Locate leukocytes (white blood cells).
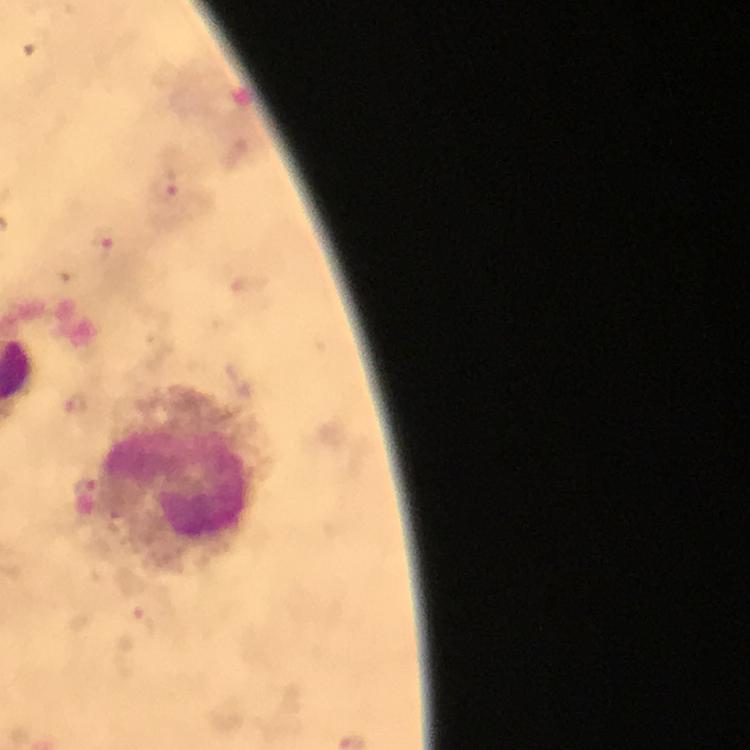

Approximate centers as {x, y} in pixels.
Leukocytes: {178, 481}.

Summary:
  - Malaria parasite locations: {164, 187}, {102, 245}, {84, 488}
  - Immersion oil: used
  - Stain: Giemsa
  - Cropped from: one field of view
  - Context: from a diagnostic examination for malaria
  - Image size: 750×750 pixels
  - Preparation: thick smear
  - Magnification: 100x
  - Capture: smartphone mounted on the microscope